Give the extent of all Plasmodium ovale-infected red blood cells.
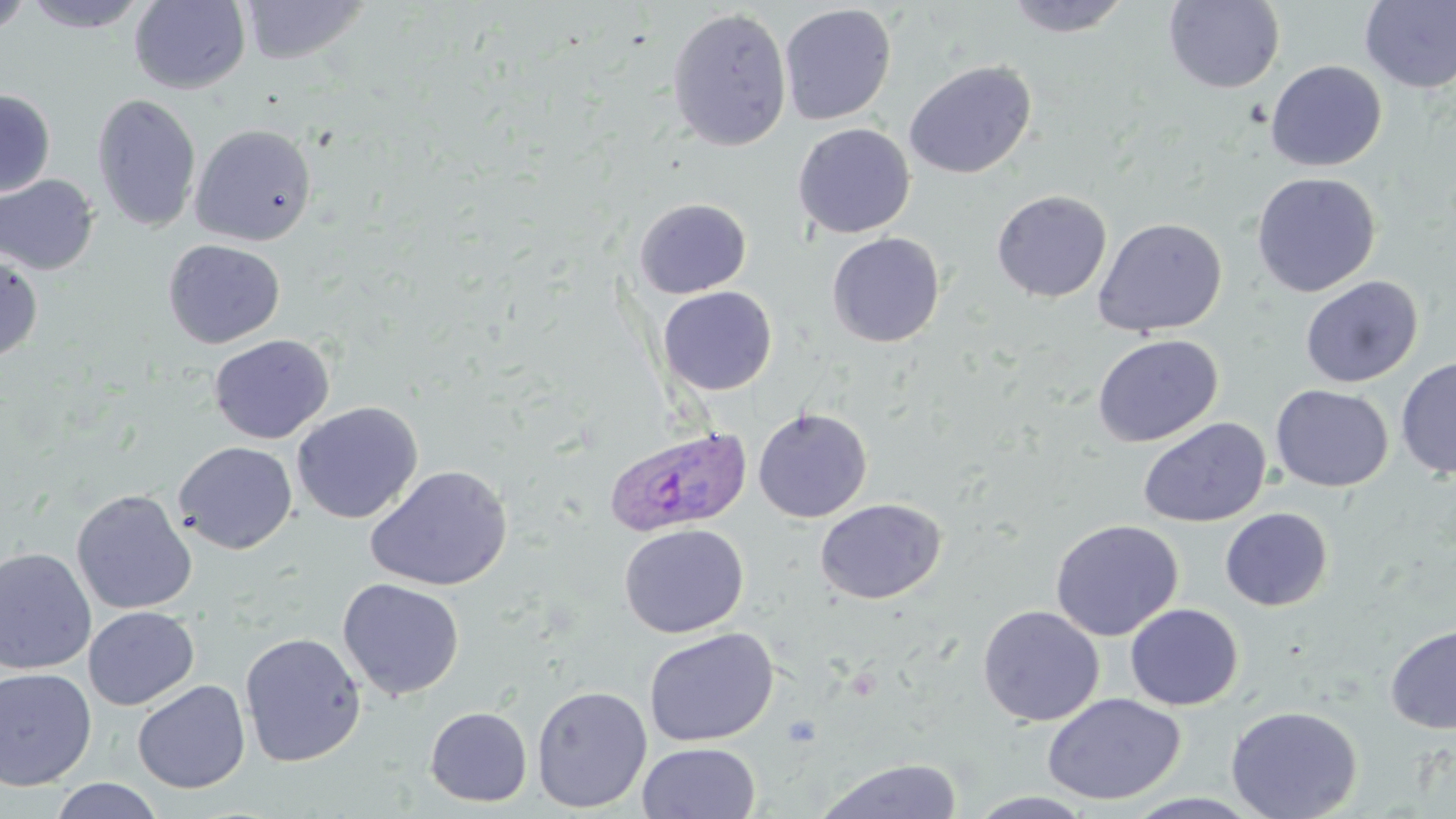

Approximate bounding boxes as (x1,y1)-(x2,y2) corner pairs in pixels.
Plasmodium ovale-infected red blood cells: (604,424)-(753,537).

slide_level_diagnosis: Plasmodium ovale
field_of_view: one of a larger specimen
modality: optical microscopy
image_size: 1456×819 pixels
preparation: thin blood film
stain: May-Grünwald-Giemsa
magnification: 1000x
uninfected_red_blood_cell_locations: 'approximate bounding boxes as (x1,y1)-(x2,y2) corner pairs in pixels: (0,0)-(36,37), (21,0)-(152,33), (129,0)-(251,94), (241,0)-(371,65), (1002,0)-(1133,38), (1164,0)-(1285,93), (1359,1)-(1456,93), (779,3)-(897,126), (666,6)-(793,152), (904,60)-(1036,179), (1266,60)-(1387,171), (0,89)-(56,198), (92,93)-(202,233), (190,123)-(317,246), (793,123)-(915,239), (1251,172)-(1381,297), (0,173)-(100,275), (991,189)-(1112,303), (634,197)-(752,299), (1092,217)-(1228,337), (826,232)-(946,347), (163,239)-(285,349), (0,253)-(43,363), (1300,276)-(1423,388), (657,286)-(778,396), (1092,333)-(1223,448), (209,334)-(335,444), (1396,356)-(1456,480), (1270,384)-(1393,492), (292,402)-(423,524), (752,407)-(872,523), (1137,416)-(1271,528), (174,441)-(297,554), (365,464)-(513,592), (71,489)-(197,615), (815,498)-(946,604), (1220,507)-(1333,611), (1050,519)-(1183,641), (619,523)-(749,639), (0,547)-(96,675), (338,578)-(464,701), (1125,603)-(1244,710), (977,605)-(1104,726), (83,606)-(199,710), (1385,624)-(1456,734), (643,628)-(778,746), (240,632)-(366,767), (0,667)-(97,790), (133,680)-(251,794), (531,685)-(652,813), (1042,693)-(1186,805), (1225,705)-(1363,819), (424,706)-(533,807), (637,741)-(761,819), (813,758)-(962,819), (48,778)-(165,819), (966,791)-(1099,818)'